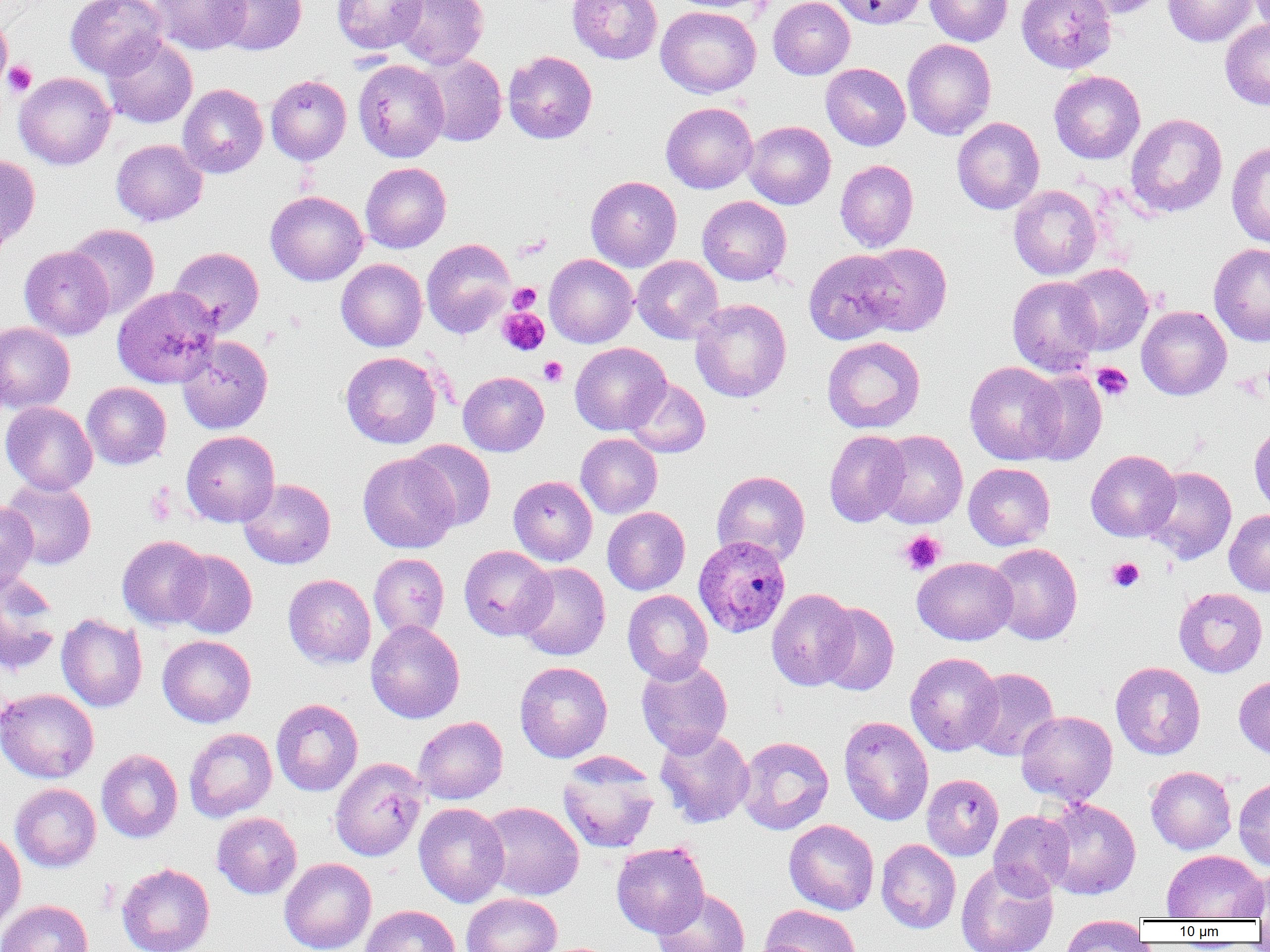
Approximate bounding boxes as (x1,y1)-(x2,y2) corner pairs in pixels. Uninfected red blood cell locations: (66,0)-(168,79), (151,0)-(250,54), (212,0)-(307,55), (331,0)-(428,54), (392,0)-(488,69), (567,0)-(662,63), (668,0)-(772,13), (768,0)-(854,79), (830,0)-(927,29), (925,0)-(1013,46), (1016,0)-(1117,74), (1070,0)-(1168,19), (1163,0)-(1256,46), (1246,0)-(1270,34), (655,6)-(761,97), (0,14)-(11,92), (1220,19)-(1270,109), (101,35)-(198,128), (902,38)-(996,139), (503,51)-(597,143), (418,53)-(506,147), (353,59)-(449,162), (821,63)-(910,150), (1049,70)-(1145,164), (14,72)-(115,169), (265,75)-(351,165), (177,84)-(268,178), (661,102)-(757,193), (1125,113)-(1227,217), (952,117)-(1045,214), (743,120)-(836,209), (111,139)-(207,226), (1226,141)-(1270,247), (0,154)-(40,250), (835,160)-(919,252), (360,162)-(451,253), (586,176)-(681,271), (1009,185)-(1102,280), (265,190)-(368,286), (697,196)-(791,286), (65,223)-(160,319), (421,238)-(515,338), (1209,242)-(1270,347), (858,243)-(952,336), (19,246)-(114,340), (169,247)-(264,335), (804,249)-(904,345), (544,254)-(638,348), (632,255)-(723,344), (336,258)-(427,351), (1062,263)-(1154,355), (1007,276)-(1103,377), (112,285)-(222,388), (690,298)-(791,403), (1136,305)-(1232,400), (0,322)-(75,413), (177,336)-(273,434), (822,336)-(925,434), (570,342)-(671,435), (340,351)-(442,449), (965,361)-(1066,464), (1021,370)-(1106,465), (458,371)-(549,456), (624,377)-(710,458), (83,382)-(171,470), (1,402)-(98,495), (1249,423)-(1270,514), (181,430)-(280,527), (824,430)-(910,527), (875,430)-(968,528), (576,433)-(662,518), (406,440)-(497,530), (1086,449)-(1181,542), (358,452)-(460,553), (963,463)-(1055,550), (1144,466)-(1236,564), (711,470)-(810,566), (508,475)-(597,566), (238,478)-(336,569), (1,479)-(97,569), (0,502)-(37,589), (602,507)-(690,595), (1224,509)-(1270,596), (117,535)-(211,629), (987,543)-(1082,644), (458,545)-(555,641), (171,549)-(257,638), (368,553)-(449,640), (912,556)-(1017,645), (515,562)-(610,660), (283,574)-(376,668), (0,575)-(62,676), (1173,587)-(1268,677), (766,588)-(858,691), (622,590)-(713,684), (816,602)-(899,695), (56,613)-(147,712), (365,620)-(465,724), (157,635)-(256,728), (905,652)-(1003,756), (636,658)-(733,757), (514,661)-(613,762), (1111,661)-(1205,760), (965,667)-(1059,761), (1234,675)-(1270,761), (0,687)-(99,783), (271,698)-(363,796), (1016,710)-(1117,805), (839,715)-(933,826), (413,716)-(508,804), (184,727)-(277,822), (654,727)-(755,828), (735,736)-(834,834), (96,749)-(183,843), (558,753)-(660,853), (330,757)-(428,861), (1146,766)-(1236,854), (922,773)-(1004,860), (1233,777)-(1270,870), (11,783)-(101,871), (1039,798)-(1140,900), (480,801)-(584,901), (413,802)-(510,907), (989,810)-(1074,899), (212,811)-(302,899), (784,819)-(879,915), (0,829)-(26,931), (876,839)-(961,933), (611,841)-(710,937), (1161,850)-(1268,921), (279,857)-(376,952), (955,860)-(1058,952), (116,862)-(215,952), (1240,868)-(1270,919), (652,889)-(750,952), (461,893)-(563,952), (0,899)-(92,952), (761,904)-(861,952), (360,905)-(460,952), (1059,916)-(1149,951). Plasmodium ovale-infected red blood cell locations: (693,535)-(790,637). Platelet locations: (2,60)-(37,97), (509,283)-(541,313), (498,308)-(549,355), (538,357)-(567,386), (1092,362)-(1133,401), (145,486)-(175,526), (898,530)-(945,575), (1107,557)-(1144,592). Slide-level diagnosis: Plasmodium ovale. Captured at 1000x magnification. Thin blood smear. Light microscopy. Single field of view. Image is 1270×952 pixels.